Report the malaria status of this cell.
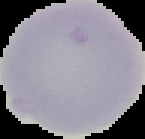

It is uninfected.

Summary:
  - Preparation: thin blood smear
  - Image size: 145×139 pixels
  - Image type: segmented cell region with the area outside set to black